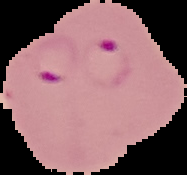
Summary:
  - Malaria status: parasitized
  - Preparation: thin blood smear
  - Image type: cell region segmented out of the field of view; surrounding area masked to black
  - Image size: 187×175 pixels